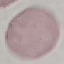

malaria status = uninfected
capture = smartphone camera at the microscope eyepiece
stain = Giemsa
image type = cell patch, automatically extracted from a larger field of view and resized to 64 × 64 pixels
preparation = thin blood smear